Report the malaria status of this cell.
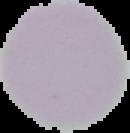
It is uninfected.

Cell region segmented out of the field of view; the surrounding area is masked to black. From a thin blood smear. Image is 130×133 pixels.